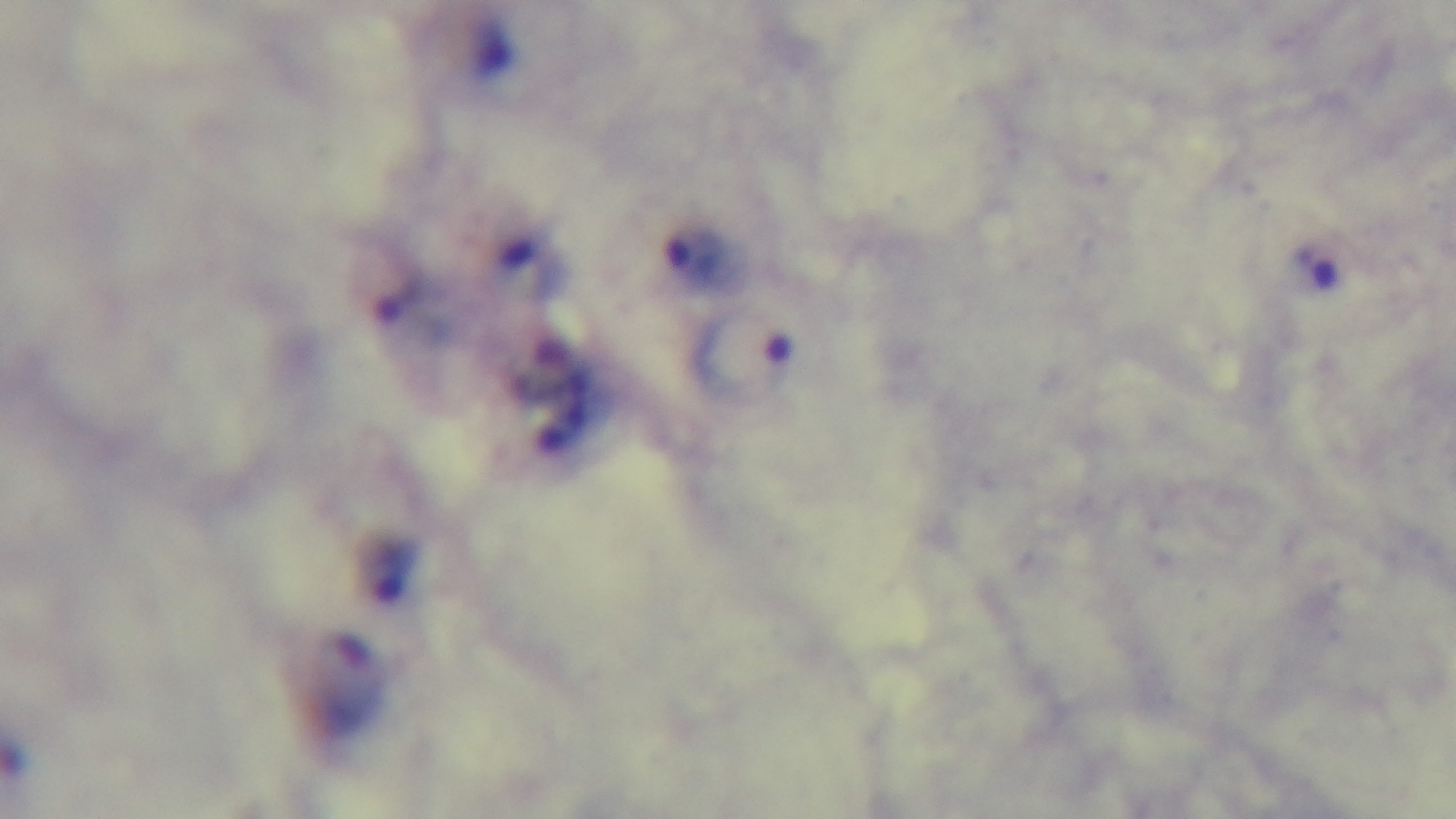
stain: Giemsa
objective: 100x oil immersion
field_of_view: single
malaria_status: positive
modality: light microscopy
preparation: thick
capture: mounted 4K digital camera